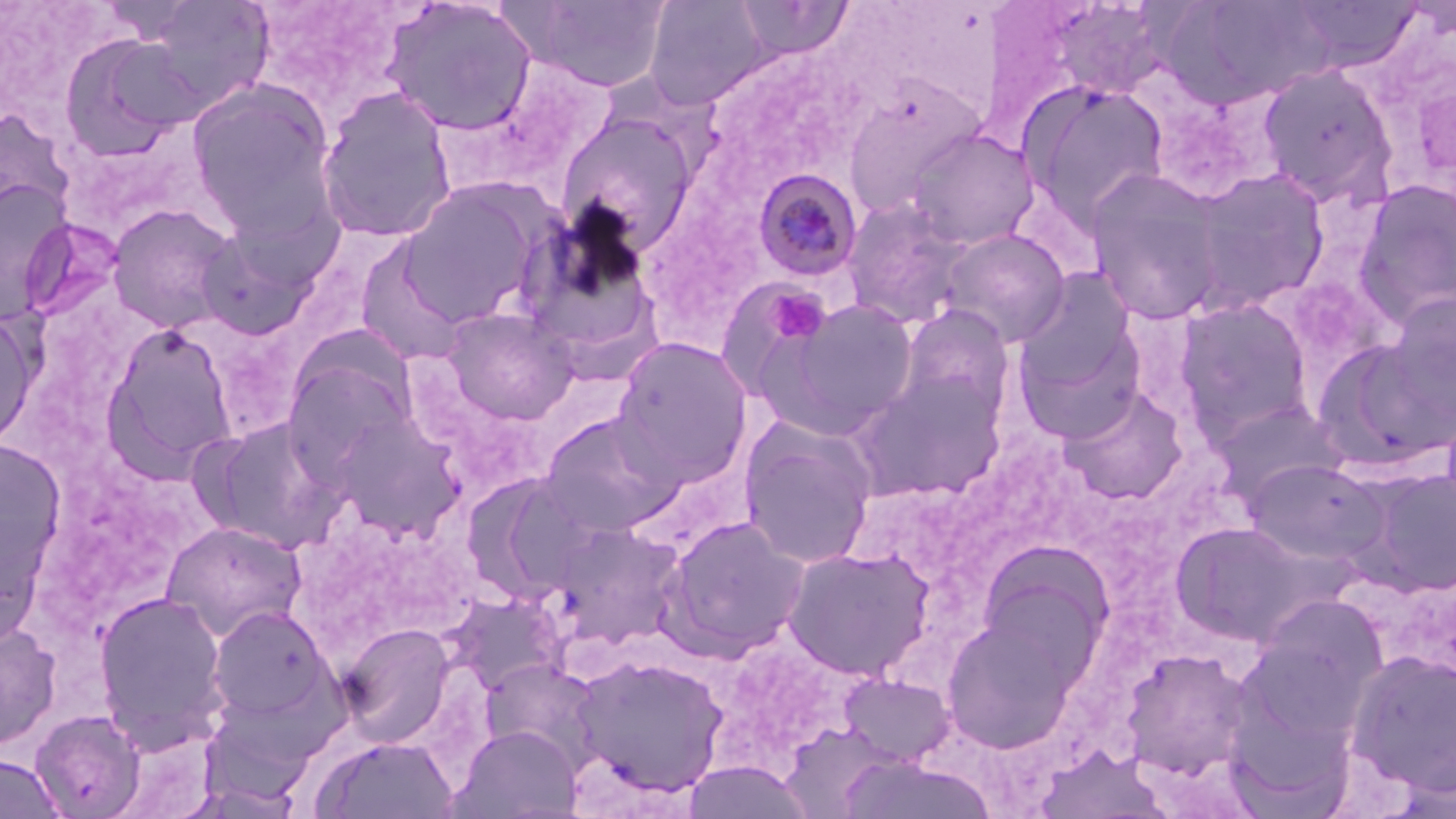
Approximate bounding boxes as [x1, y1, x2, y2] in pixels. Platelet locations: [757, 286, 830, 344]. Plasmodium malariae-infected red blood cell locations: [753, 169, 864, 282]. Uninfected red blood cell locations: [381, 0, 538, 137], [519, 0, 671, 92], [644, 0, 774, 107], [1283, 0, 1422, 73], [141, 1, 275, 117], [734, 1, 852, 61], [1168, 1, 1338, 108], [1046, 2, 1171, 100], [57, 33, 198, 160], [1257, 63, 1400, 207], [187, 79, 339, 234], [842, 80, 987, 215], [1019, 81, 1170, 230], [315, 87, 457, 243], [0, 107, 75, 226], [557, 112, 698, 248], [904, 127, 1041, 250], [1189, 167, 1331, 311], [1084, 169, 1228, 325], [1353, 179, 1456, 327], [0, 180, 75, 322], [399, 182, 549, 327], [839, 197, 972, 329], [515, 203, 665, 360], [107, 204, 241, 334], [194, 221, 327, 341], [938, 228, 1071, 347], [355, 239, 469, 367], [1015, 268, 1141, 400], [1383, 292, 1456, 427], [768, 297, 921, 436], [1174, 298, 1316, 441], [898, 305, 1014, 419], [442, 307, 578, 424], [0, 308, 40, 451], [1014, 319, 1147, 443], [101, 324, 238, 477], [611, 336, 753, 483], [1316, 337, 1454, 470], [281, 353, 416, 480], [856, 371, 1006, 501], [1061, 386, 1188, 504], [1208, 398, 1347, 505], [327, 409, 467, 542], [540, 411, 683, 537], [195, 417, 341, 552], [738, 418, 878, 569], [0, 438, 67, 593], [1242, 458, 1385, 565], [1361, 468, 1456, 596], [469, 474, 600, 603], [660, 515, 810, 659], [161, 520, 306, 642], [1170, 521, 1310, 646], [548, 522, 685, 647], [782, 546, 933, 680], [974, 551, 1112, 693], [93, 590, 231, 751], [450, 592, 566, 694], [1244, 597, 1388, 739], [207, 604, 333, 725], [941, 609, 1082, 752], [336, 622, 455, 749], [0, 623, 61, 749], [1122, 647, 1251, 779], [1346, 649, 1456, 794], [571, 655, 729, 798], [478, 657, 605, 770], [839, 672, 955, 768], [30, 709, 147, 818], [451, 724, 583, 818], [312, 735, 459, 818], [1036, 746, 1175, 818], [0, 754, 66, 819]. Slide-level diagnosis: Plasmodium malariae. Image is 1456×819 pixels. 1000x magnification. Light microscopy. Thin blood film. Single field of view. May-Grünwald-Giemsa-stained preparation.